Locate every uninfected red blood cell.
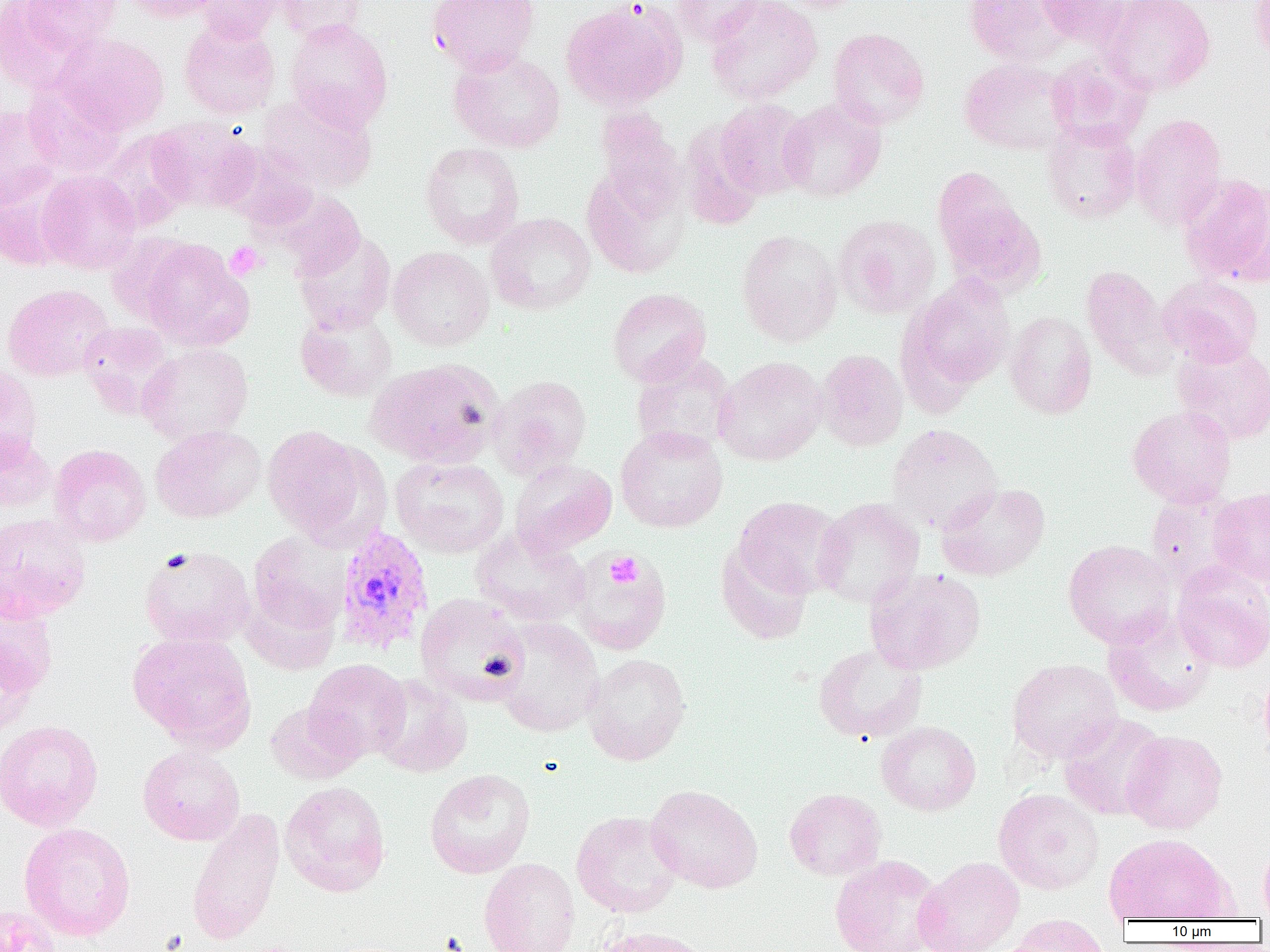

Approximate bounding boxes as [x1, y1, x2, y2] in pixels.
Uninfected red blood cells: [18, 0, 122, 56], [121, 0, 224, 23], [196, 0, 284, 44], [274, 0, 368, 42], [428, 0, 540, 75], [671, 0, 765, 46], [705, 0, 822, 104], [771, 0, 870, 13], [963, 0, 1071, 67], [1035, 0, 1134, 47], [1101, 0, 1215, 95], [1250, 0, 1270, 66], [1, 1, 86, 93], [560, 1, 685, 111], [285, 18, 393, 131], [179, 20, 280, 119], [827, 28, 930, 130], [53, 32, 169, 135], [448, 48, 566, 153], [1046, 52, 1152, 148], [959, 58, 1073, 155], [23, 78, 127, 177], [257, 91, 378, 194], [715, 99, 813, 200], [778, 99, 887, 202], [0, 106, 63, 209], [592, 108, 686, 218], [1130, 113, 1227, 231], [147, 117, 258, 212], [1041, 119, 1143, 225], [96, 131, 194, 230], [420, 142, 525, 248], [931, 166, 1043, 292], [583, 169, 689, 279], [36, 170, 141, 274], [1179, 173, 1270, 285], [0, 181, 70, 270], [274, 191, 366, 279], [486, 213, 596, 315], [835, 214, 940, 319], [293, 228, 396, 334], [736, 229, 843, 347], [137, 238, 253, 351], [388, 246, 494, 351], [1081, 265, 1178, 380], [902, 275, 1015, 396], [1158, 275, 1264, 367], [2, 284, 114, 382], [607, 287, 712, 387], [295, 307, 397, 402], [1004, 311, 1097, 419], [77, 321, 175, 419], [1171, 342, 1270, 445], [137, 343, 254, 444], [815, 349, 908, 451], [630, 351, 735, 457], [714, 356, 828, 466], [366, 358, 505, 468], [0, 363, 43, 466], [489, 374, 592, 480], [1127, 405, 1236, 508], [886, 423, 1002, 533], [150, 425, 266, 523], [261, 425, 375, 542], [615, 425, 728, 532], [0, 432, 55, 514], [49, 444, 151, 546], [390, 456, 509, 557], [510, 459, 617, 555], [936, 482, 1051, 581], [1208, 487, 1270, 587], [1146, 492, 1249, 591], [734, 496, 845, 597], [813, 498, 924, 609], [0, 513, 92, 622], [470, 527, 591, 626], [249, 531, 352, 632], [716, 539, 814, 645], [1063, 539, 1177, 648], [139, 545, 255, 648], [570, 551, 672, 655], [1172, 562, 1270, 673], [865, 567, 985, 675], [241, 588, 341, 675], [0, 594, 58, 697], [414, 594, 531, 705], [1102, 609, 1217, 717], [492, 617, 604, 737], [128, 632, 256, 749], [0, 638, 41, 740], [813, 643, 928, 743], [583, 653, 691, 765], [1007, 658, 1123, 764], [304, 659, 411, 762], [1258, 664, 1270, 766], [370, 674, 473, 777], [265, 701, 362, 785], [1059, 713, 1169, 820], [0, 719, 103, 831], [876, 721, 981, 816], [1122, 730, 1227, 834], [138, 745, 245, 846], [424, 768, 536, 879], [280, 781, 391, 897], [646, 785, 763, 893], [784, 788, 886, 881], [993, 788, 1104, 895], [186, 808, 285, 946], [571, 810, 684, 918], [19, 822, 136, 941], [1105, 832, 1233, 921], [1258, 840, 1270, 919], [830, 855, 944, 952], [913, 856, 1025, 952], [479, 857, 580, 952], [0, 904, 63, 952], [1004, 913, 1112, 951], [591, 925, 714, 952].

Platelet locations: [225, 242, 265, 280], [605, 551, 643, 589]. Plasmodium vivax-infected red blood cell locations: [334, 526, 433, 656]. Slide-level diagnosis: Plasmodium vivax. Light microscopy. One field of a larger specimen. Captured at 1000x magnification. Image is 1270×952 pixels. Thin blood smear.